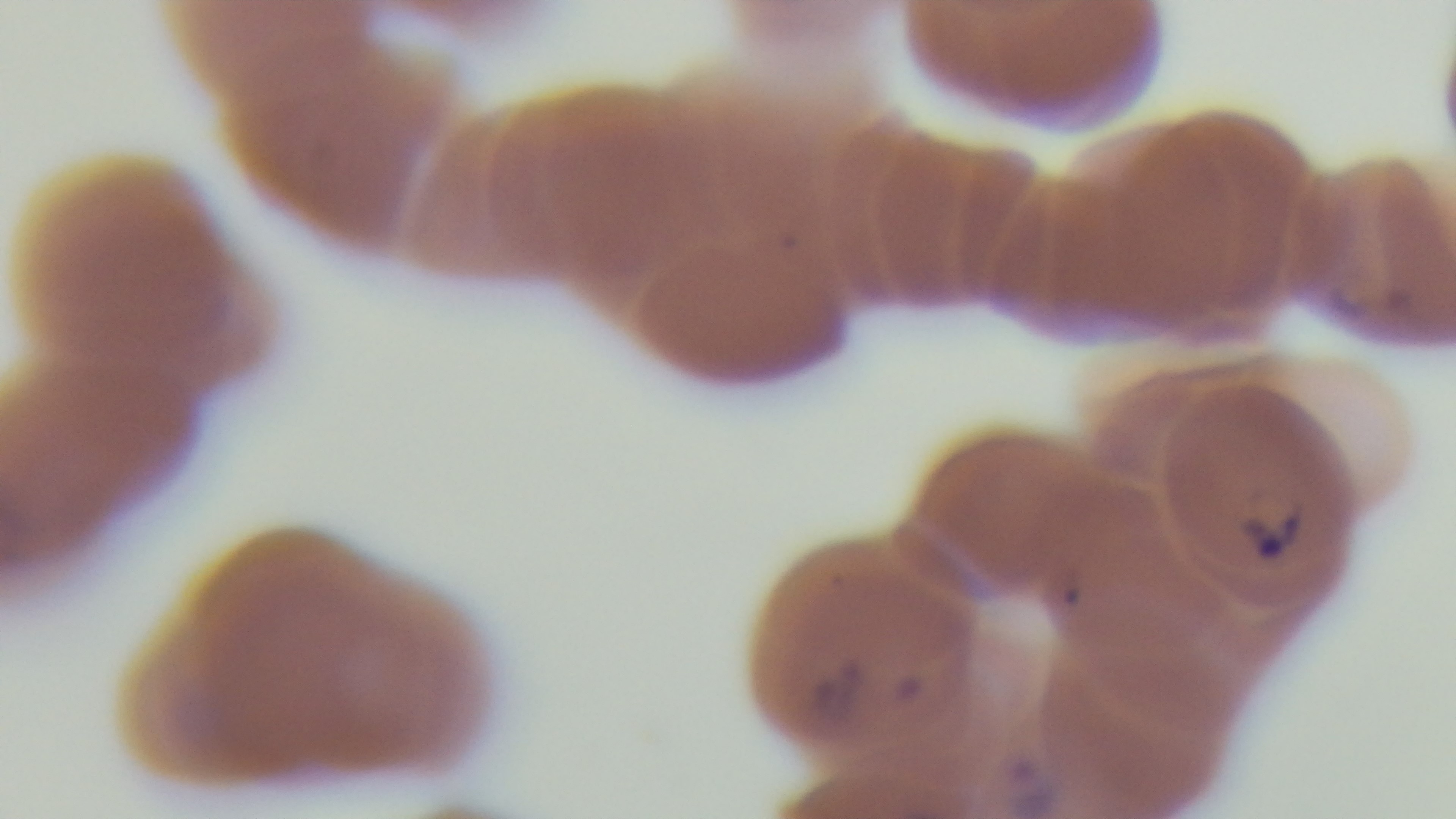
modality = light microscopy
objective = 100x oil immersion
preparation = thin blood film
field of view = one from the slide
capture = mounted 4K digital camera
malaria status = positive
stain = Giemsa